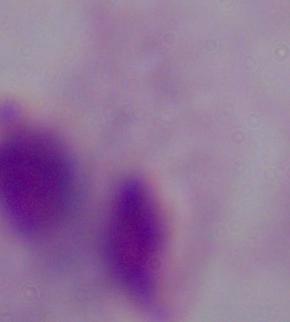
Photomicrograph. A trichomonad is shown. Captured at 1000x magnification.